Assess the morphology of the red blood cells.
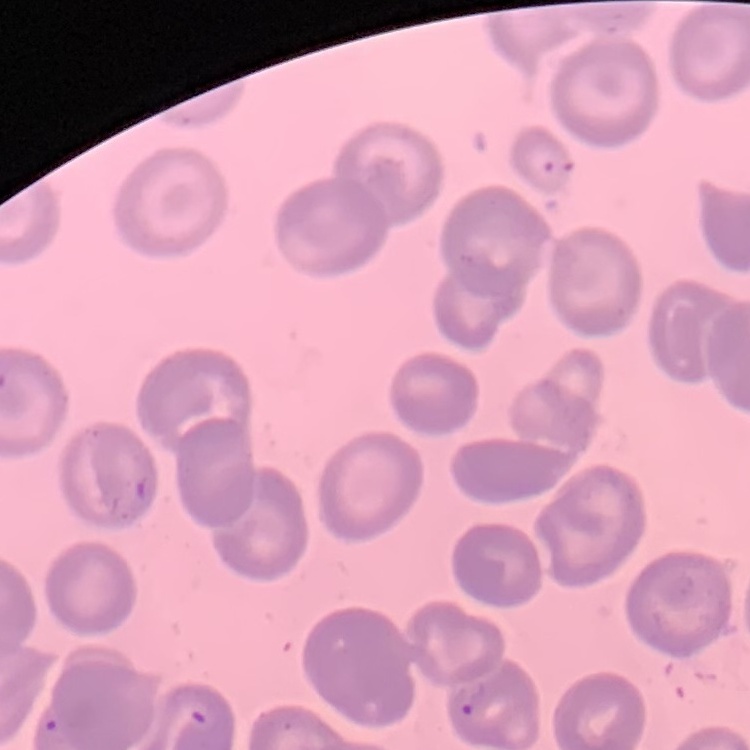
No rouleaux formation.

Field's or Giemsa stain. Thin peripheral smear. One tile cut from a larger photomicrograph.